Locate every Plasmodium malariae-infected red blood cell.
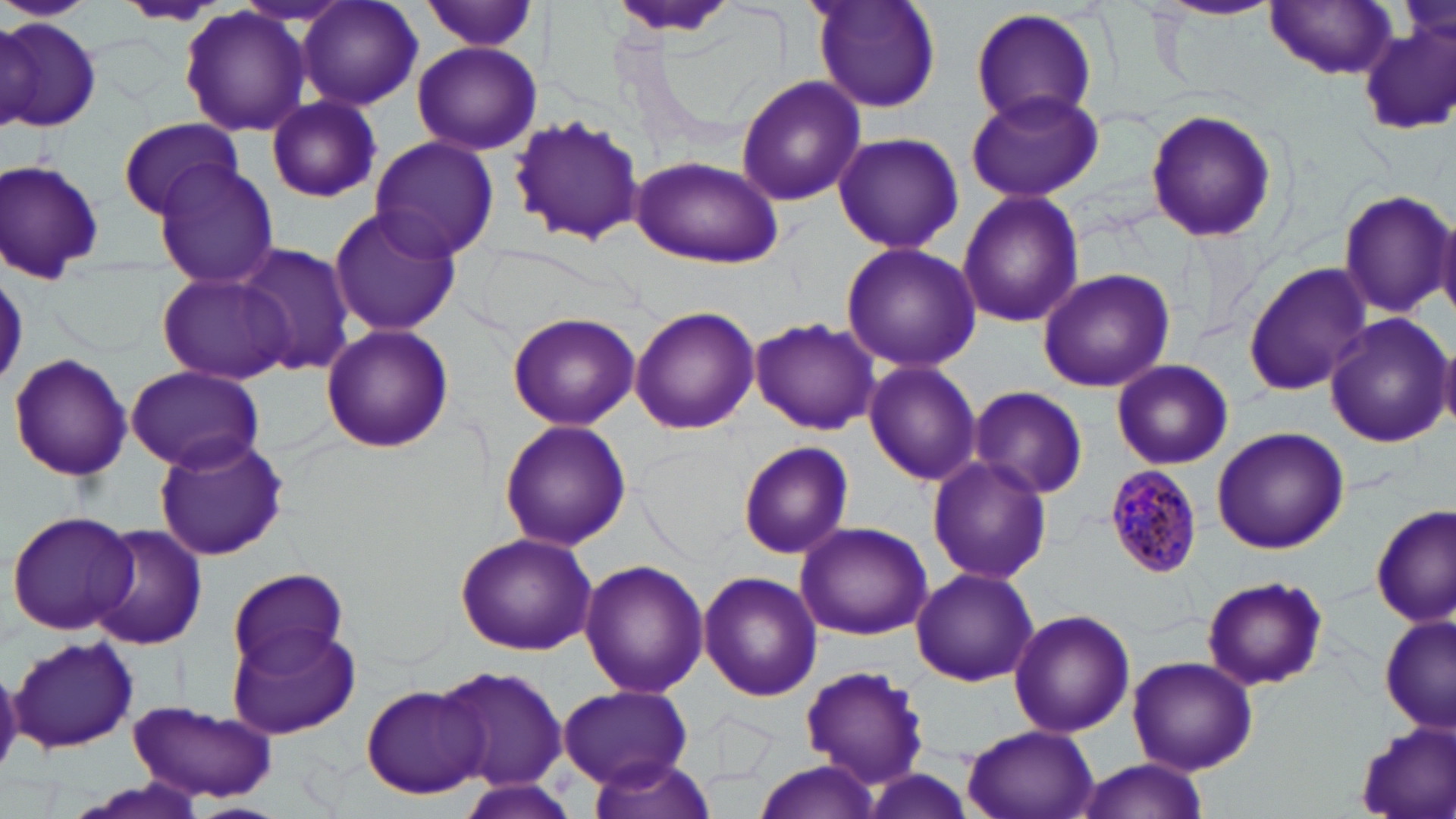

Approximate bounding boxes as (x1,y1)-(x2,y2) corner pairs in pixels.
Plasmodium malariae-infected red blood cells: (1098,463)-(1205,582).

slide-level diagnosis = Plasmodium malariae
image size = 1456×819 pixels
preparation = thin blood film
modality = light microscopy
magnification = 1000x
stain = May-Grünwald-Giemsa
uninfected red blood cell locations = approximate bounding boxes as (x1,y1)-(x2,y2) corner pairs in pixels: (0,0)-(91,23), (298,0)-(424,112), (809,0)-(942,115), (609,1)-(741,38), (1267,1)-(1399,79), (115,2)-(226,26), (420,3)-(542,51), (969,6)-(1100,128), (177,7)-(310,138), (0,17)-(105,133), (1358,18)-(1453,136), (413,40)-(542,155), (735,75)-(866,208), (965,88)-(1102,203), (264,96)-(383,204), (1144,109)-(1279,245), (506,112)-(649,249), (118,118)-(243,217), (833,131)-(964,255), (370,136)-(499,261), (0,157)-(106,283), (631,157)-(784,269), (152,159)-(283,290), (1337,189)-(1454,320), (956,191)-(1086,329), (327,204)-(463,339), (1435,208)-(1456,327), (840,242)-(983,373), (236,243)-(358,376), (1242,262)-(1372,396), (1037,268)-(1175,392), (157,270)-(295,384), (630,306)-(760,435), (506,312)-(639,429), (1324,314)-(1455,447), (748,316)-(881,434), (321,323)-(453,453), (1436,338)-(1456,436), (8,351)-(133,480), (1110,358)-(1234,470), (863,359)-(981,485), (124,365)-(263,473), (967,388)-(1088,500), (499,420)-(630,552), (1211,426)-(1349,556), (153,433)-(290,561), (737,440)-(854,560), (926,454)-(1052,587), (1370,503)-(1455,628), (6,509)-(141,638), (794,520)-(934,640), (88,525)-(209,650), (455,533)-(597,655), (580,559)-(709,698), (228,567)-(348,675), (910,567)-(1039,687), (698,571)-(822,702), (1201,576)-(1328,691), (1007,608)-(1135,738), (1378,613)-(1454,735), (227,624)-(360,739), (9,636)-(140,754), (1127,656)-(1257,773), (800,662)-(930,788), (432,665)-(571,791), (0,671)-(22,770), (361,681)-(489,799), (558,684)-(691,788), (129,702)-(279,801), (958,722)-(1099,819), (1352,722)-(1456,819), (580,752)-(715,819), (751,756)-(885,817), (1067,757)-(1212,817), (859,769)-(979,819), (461,778)-(581,819)
field of view = one of a larger specimen